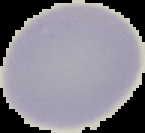

image_type: segmented cell region on a black background
malaria_status: uninfected
image_size: 145×133 pixels
preparation: thin blood smear